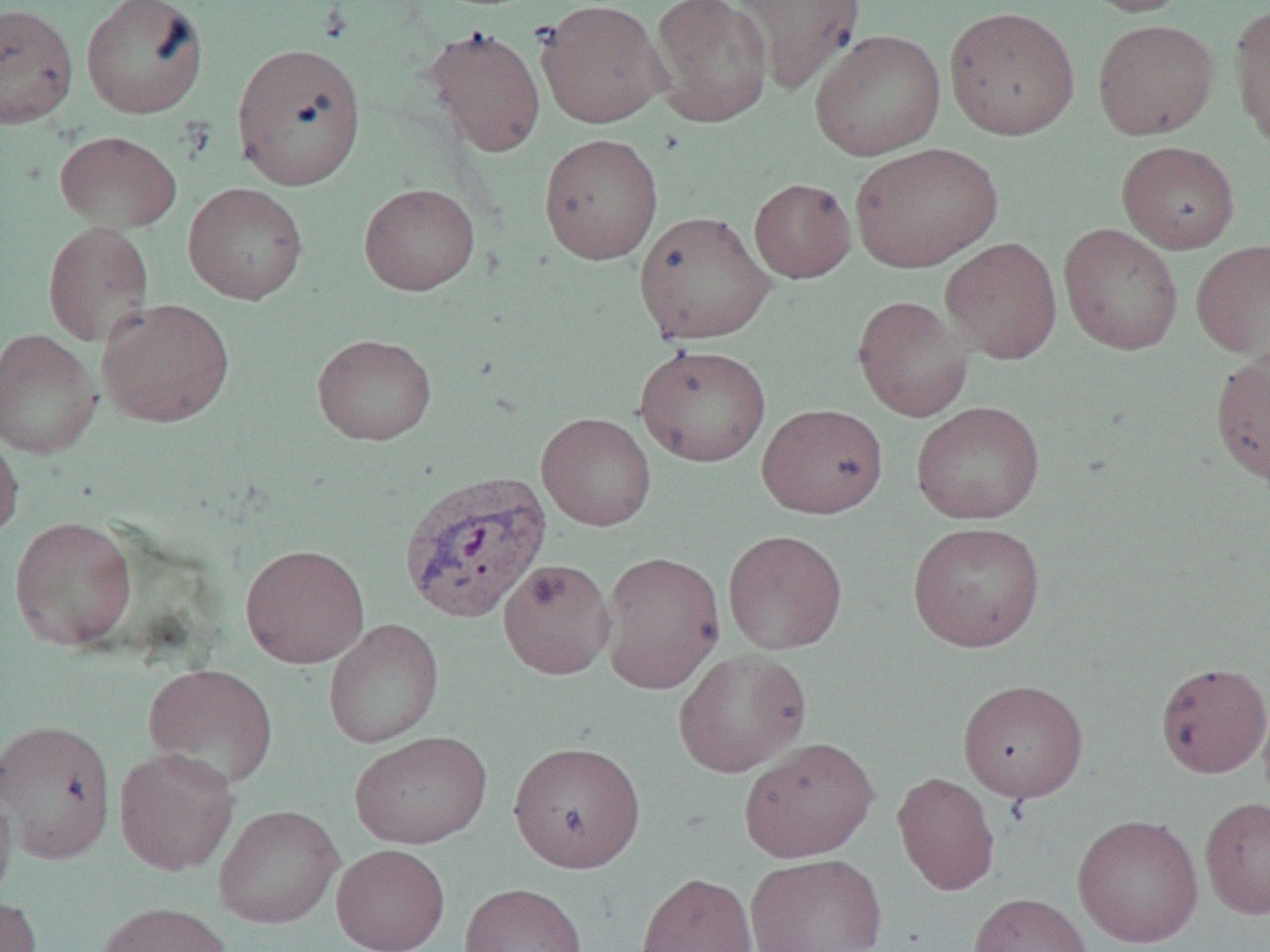
slide_level_diagnosis: Plasmodium vivax
image_size: 1270×952 pixels
modality: light microscopy
uninfected_red_blood_cell_locations: 'approximate bounding boxes as (x1,y1)-(x2,y2) corner pairs in pixels: (81,0)-(209,119), (649,0)-(773,129), (732,0)-(865,95), (1073,0)-(1194,16), (535,1)-(669,129), (0,2)-(79,129), (1229,4)-(1270,150), (944,5)-(1080,141), (1092,19)-(1220,140), (425,24)-(546,158), (809,29)-(946,161), (232,42)-(367,190), (55,130)-(182,233), (539,133)-(663,265), (1117,140)-(1240,253), (850,141)-(1003,272), (749,178)-(856,283), (184,182)-(308,304), (359,182)-(480,295), (634,210)-(774,344), (42,221)-(155,347), (1059,223)-(1183,355), (940,236)-(1062,364), (1190,239)-(1270,360), (852,295)-(973,422), (96,298)-(235,428), (0,328)-(102,459), (312,333)-(437,445), (635,344)-(772,467), (1210,349)-(1270,485), (911,401)-(1045,524), (757,403)-(888,518), (537,412)-(657,531), (0,429)-(24,544), (9,516)-(138,651), (908,521)-(1046,652), (723,530)-(848,654), (240,544)-(370,668), (599,550)-(725,694), (498,558)-(616,680), (323,618)-(444,748), (673,647)-(811,778), (1156,661)-(1270,777), (143,663)-(279,789), (957,678)-(1088,802), (1,719)-(117,864), (350,730)-(492,849), (739,736)-(879,862), (508,740)-(646,873), (114,746)-(239,875), (893,771)-(1000,896), (0,782)-(16,906), (1199,796)-(1270,920), (214,804)-(344,928), (1072,812)-(1204,947), (331,843)-(451,952), (745,853)-(888,951), (636,871)-(757,952), (459,882)-(587,952), (968,892)-(1093,952), (0,894)-(43,952), (95,901)-(234,952)'
preparation: thin blood smear
magnification: 1000x
plasmodium_vivax_infected_red_blood_cell_locations: 'approximate bounding boxes as (x1,y1)-(x2,y2) corner pairs in pixels: (398,469)-(553,623)'
field_of_view: single